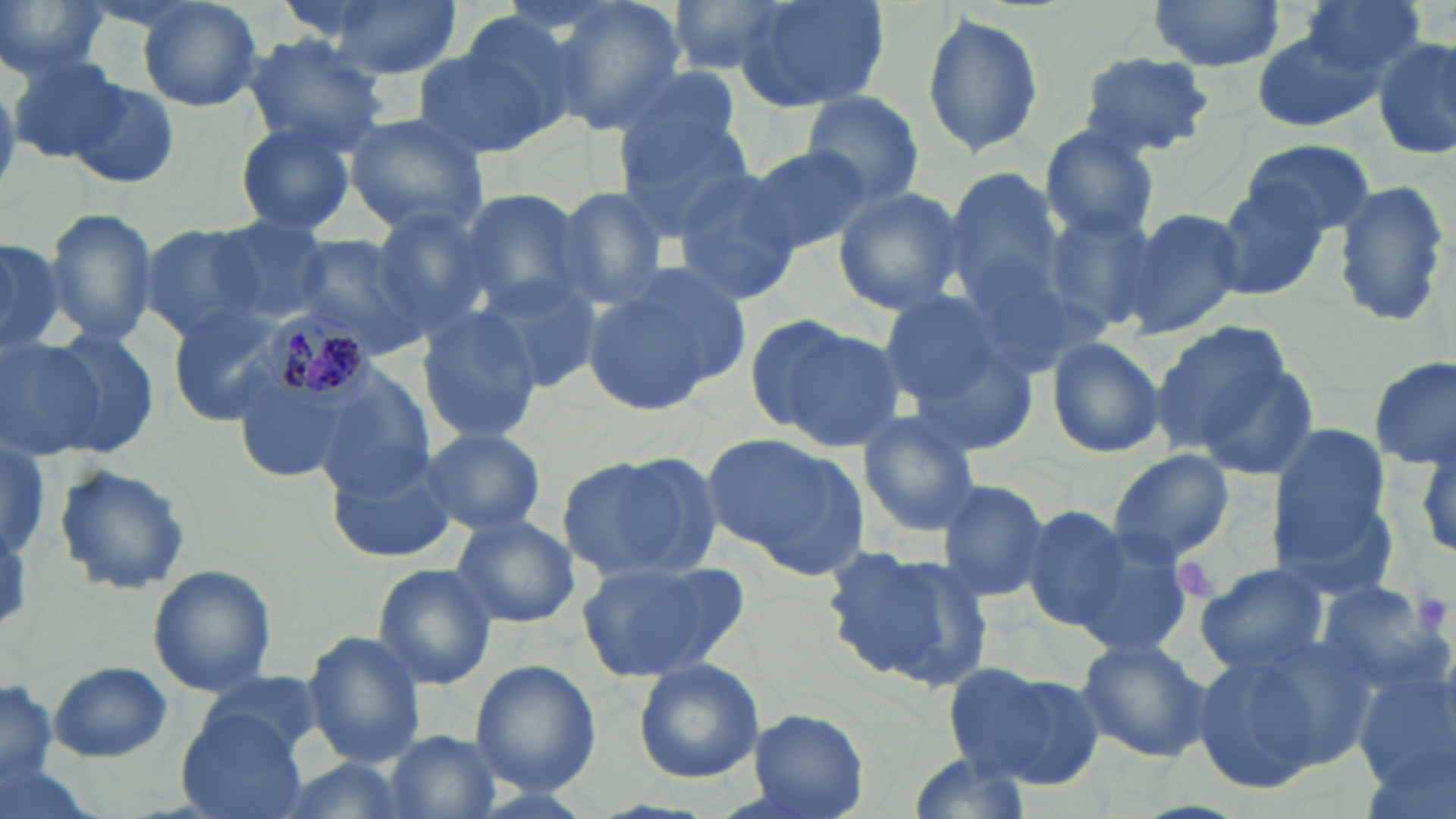

Summary:
  - Coordinate format: approximate bounding boxes as named x1/y1/x2/y2 corners in pixels
  - Platelet locations: (x1=1410, y1=590, x2=1452, y2=637)
  - Plasmodium malariae-infected red blood cell locations: (x1=266, y1=310, x2=377, y2=414)
  - Uninfected red blood cell locations: (x1=139, y1=0, x2=264, y2=112), (x1=311, y1=0, x2=465, y2=78), (x1=539, y1=0, x2=687, y2=138), (x1=663, y1=0, x2=793, y2=75), (x1=733, y1=0, x2=889, y2=113), (x1=1146, y1=0, x2=1288, y2=74), (x1=1292, y1=0, x2=1426, y2=88), (x1=0, y1=1, x2=109, y2=83), (x1=456, y1=8, x2=592, y2=138), (x1=919, y1=13, x2=1045, y2=158), (x1=1247, y1=29, x2=1381, y2=132), (x1=1374, y1=33, x2=1456, y2=160), (x1=239, y1=34, x2=389, y2=155), (x1=410, y1=37, x2=560, y2=163), (x1=1074, y1=51, x2=1218, y2=158), (x1=7, y1=54, x2=125, y2=162), (x1=376, y1=58, x2=529, y2=210), (x1=611, y1=61, x2=748, y2=169), (x1=60, y1=76, x2=182, y2=191), (x1=801, y1=91, x2=925, y2=206), (x1=612, y1=110, x2=757, y2=239), (x1=342, y1=115, x2=490, y2=239), (x1=232, y1=118, x2=360, y2=238), (x1=1038, y1=123, x2=1163, y2=244), (x1=1239, y1=137, x2=1379, y2=239), (x1=742, y1=143, x2=874, y2=255), (x1=671, y1=169, x2=803, y2=306), (x1=945, y1=170, x2=1065, y2=300), (x1=1204, y1=177, x2=1328, y2=298), (x1=1331, y1=178, x2=1451, y2=330), (x1=548, y1=186, x2=673, y2=311), (x1=831, y1=187, x2=967, y2=315), (x1=456, y1=188, x2=592, y2=322), (x1=40, y1=207, x2=159, y2=350), (x1=366, y1=207, x2=494, y2=334), (x1=1044, y1=208, x2=1162, y2=334), (x1=1125, y1=208, x2=1246, y2=338), (x1=202, y1=220, x2=336, y2=322), (x1=141, y1=225, x2=269, y2=340), (x1=286, y1=233, x2=430, y2=358), (x1=0, y1=234, x2=68, y2=354), (x1=953, y1=253, x2=1102, y2=377), (x1=583, y1=262, x2=750, y2=414), (x1=473, y1=271, x2=601, y2=393), (x1=873, y1=288, x2=1029, y2=420), (x1=168, y1=303, x2=297, y2=422), (x1=415, y1=306, x2=544, y2=445), (x1=746, y1=314, x2=904, y2=453), (x1=1149, y1=321, x2=1297, y2=455), (x1=38, y1=328, x2=162, y2=453), (x1=0, y1=336, x2=118, y2=460), (x1=1044, y1=337, x2=1167, y2=459), (x1=903, y1=340, x2=1043, y2=458), (x1=1370, y1=356, x2=1454, y2=469), (x1=1196, y1=360, x2=1322, y2=479), (x1=314, y1=365, x2=438, y2=496), (x1=855, y1=410, x2=984, y2=536), (x1=417, y1=426, x2=548, y2=536), (x1=1269, y1=428, x2=1390, y2=566), (x1=706, y1=433, x2=870, y2=578), (x1=1405, y1=436, x2=1456, y2=564), (x1=0, y1=442, x2=51, y2=566), (x1=324, y1=447, x2=462, y2=562), (x1=1106, y1=450, x2=1235, y2=564), (x1=557, y1=452, x2=718, y2=580), (x1=53, y1=462, x2=193, y2=595), (x1=934, y1=479, x2=1050, y2=605), (x1=1276, y1=500, x2=1402, y2=605), (x1=1017, y1=504, x2=1147, y2=635), (x1=449, y1=514, x2=580, y2=630), (x1=1057, y1=521, x2=1201, y2=662), (x1=821, y1=544, x2=994, y2=693), (x1=575, y1=557, x2=751, y2=682), (x1=1194, y1=561, x2=1331, y2=675), (x1=371, y1=562, x2=498, y2=689), (x1=148, y1=565, x2=276, y2=696), (x1=1311, y1=579, x2=1449, y2=694), (x1=303, y1=632, x2=428, y2=767), (x1=1075, y1=638, x2=1213, y2=763), (x1=1189, y1=647, x2=1343, y2=798), (x1=469, y1=659, x2=600, y2=795), (x1=633, y1=659, x2=763, y2=784), (x1=48, y1=661, x2=173, y2=761), (x1=1355, y1=662, x2=1456, y2=794), (x1=946, y1=664, x2=1104, y2=790), (x1=198, y1=673, x2=325, y2=764), (x1=0, y1=682, x2=59, y2=788), (x1=747, y1=707, x2=869, y2=818), (x1=179, y1=711, x2=311, y2=819), (x1=387, y1=730, x2=499, y2=818), (x1=902, y1=753, x2=1034, y2=818), (x1=268, y1=757, x2=411, y2=819)
  - Slide-level diagnosis: Plasmodium malariae
  - Magnification: 1000x
  - Modality: light microscopy
  - Preparation: thin blood film
  - Image size: 1456×819 pixels
  - Field of view: one of a larger specimen
  - Stain: May-Grünwald-Giemsa